Classify this cell by malaria status.
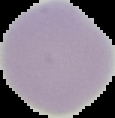
Uninfected.

{
  "image_size": "115×118 pixels",
  "preparation": "thin blood film",
  "image_type": "cell region segmented out of the field of view; surrounding area masked to black"
}